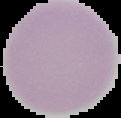

image size = 121×118 pixels
malaria status = uninfected
image type = cell region segmented out of the field of view; surrounding area masked to black
preparation = thin blood smear